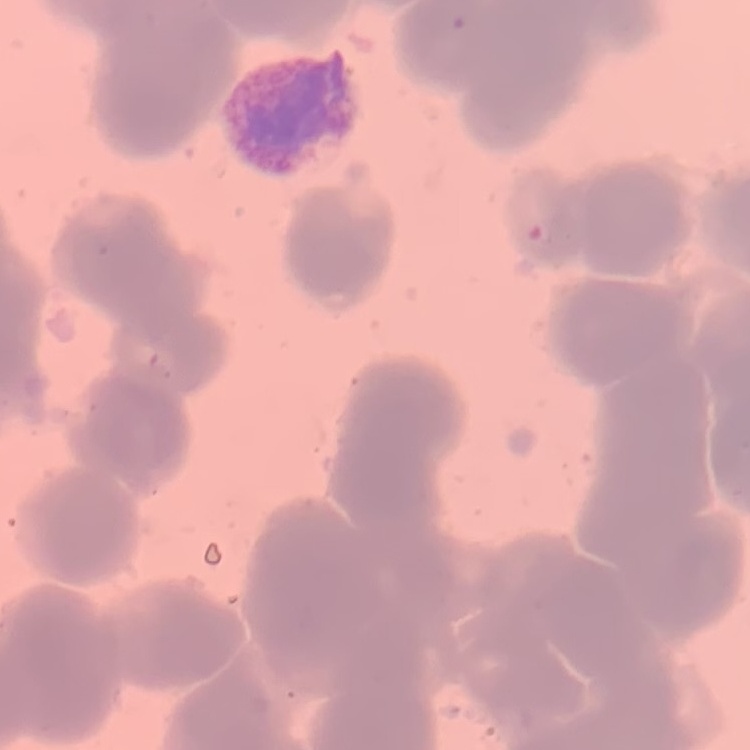

Summary:
  - Red blood cell morphology: rouleaux formation
  - Stain: Field's or Giemsa
  - Image type: square crop of a larger photomicrograph
  - Preparation: thin blood film